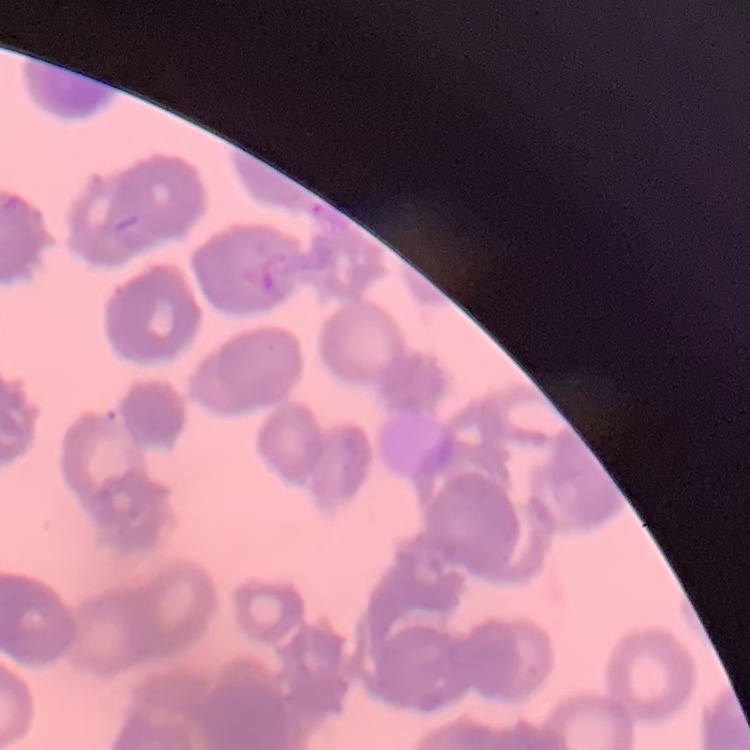 The erythrocytes exhibit rouleaux formation. Field's or Giemsa stain. One tile cut from a larger photomicrograph. Thin blood smear.